Report the malaria status of this cell.
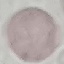

Uninfected.

Giemsa stain. Thin smear of blood. Cell patch, automatically extracted from a larger field of view and resized to 64 × 64 pixels. Acquired by smartphone through the microscope eyepiece.